Report the malaria status of this cell.
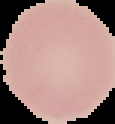

Uninfected.

The area outside the segmented cell region is set to black. Image is 115×124 pixels. From a thin blood film.